Classify this cell by malaria status.
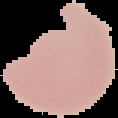
Uninfected.

{
  "image_type": "segmented cell region on a black background",
  "preparation": "thin blood film",
  "image_size": "118×118 pixels"
}